Identify the cell.
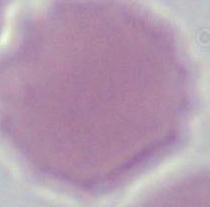

An erythrocyte.

modality = photomicrograph
magnification = 1000x